Give a bounding box for every Plasmodium parasite, every leukocyte, and every artifact (stain precipitate or debris).
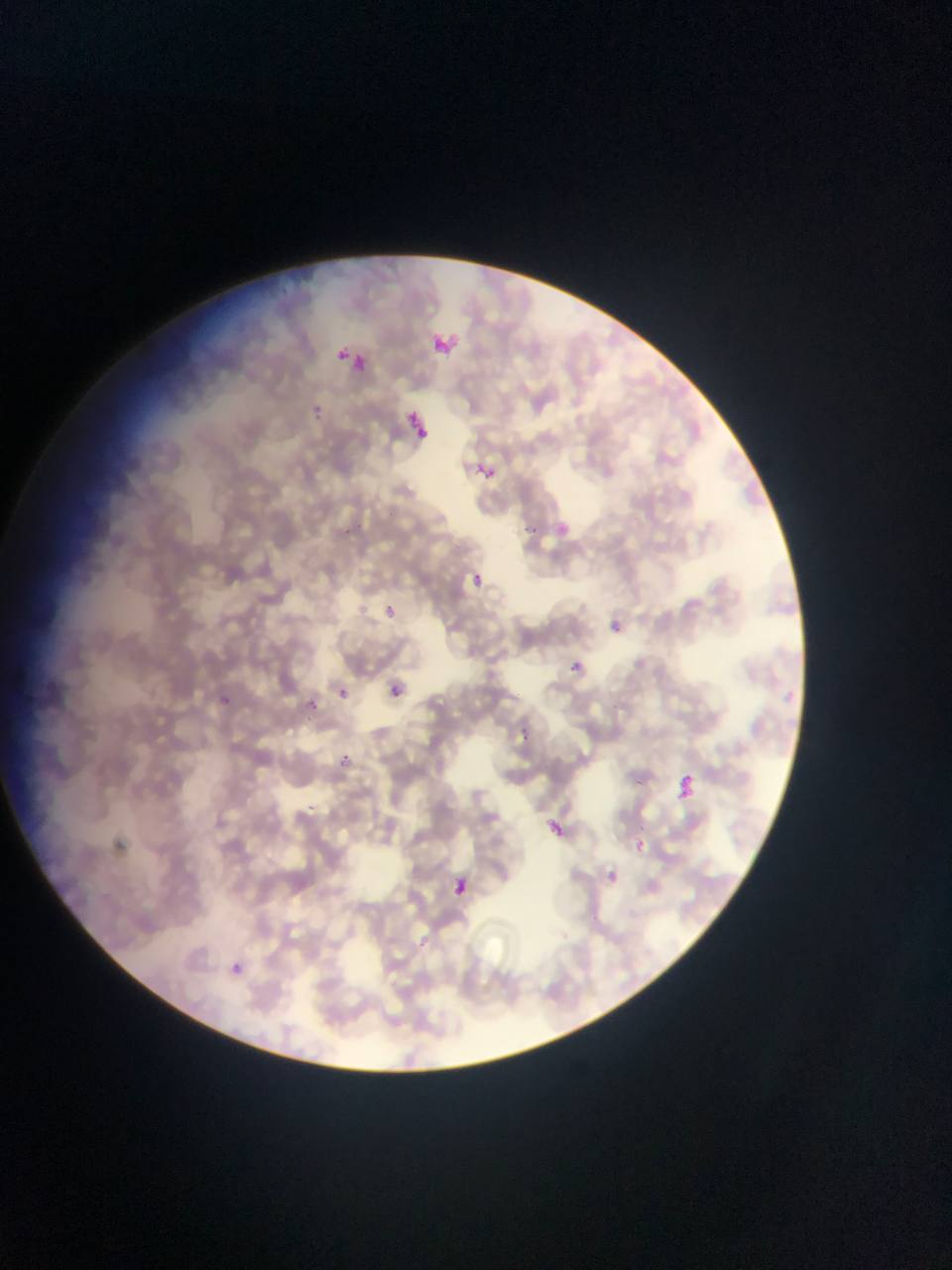

Approximate bounding boxes as left top right bottom in pixels.
Plasmodium parasites: 426 313 482 351; 342 351 397 389; 313 402 322 421; 408 405 436 446; 468 448 494 486; 354 519 364 533; 527 523 542 536; 345 525 355 541; 469 570 487 588; 381 605 394 618; 602 615 626 638; 566 658 588 678; 383 681 406 702; 332 684 352 703; 308 695 318 712; 222 696 241 717; 516 723 527 738; 341 752 356 765; 671 775 699 805; 542 815 569 842; 627 836 650 858; 599 865 624 891; 444 873 474 900; 219 952 253 986.
No leukocytes observed.

image_size: 952×1270 pixels
preparation: thin blood smear
country: Ghana
field_of_view: single
capture: mobile-phone photograph through a microscope